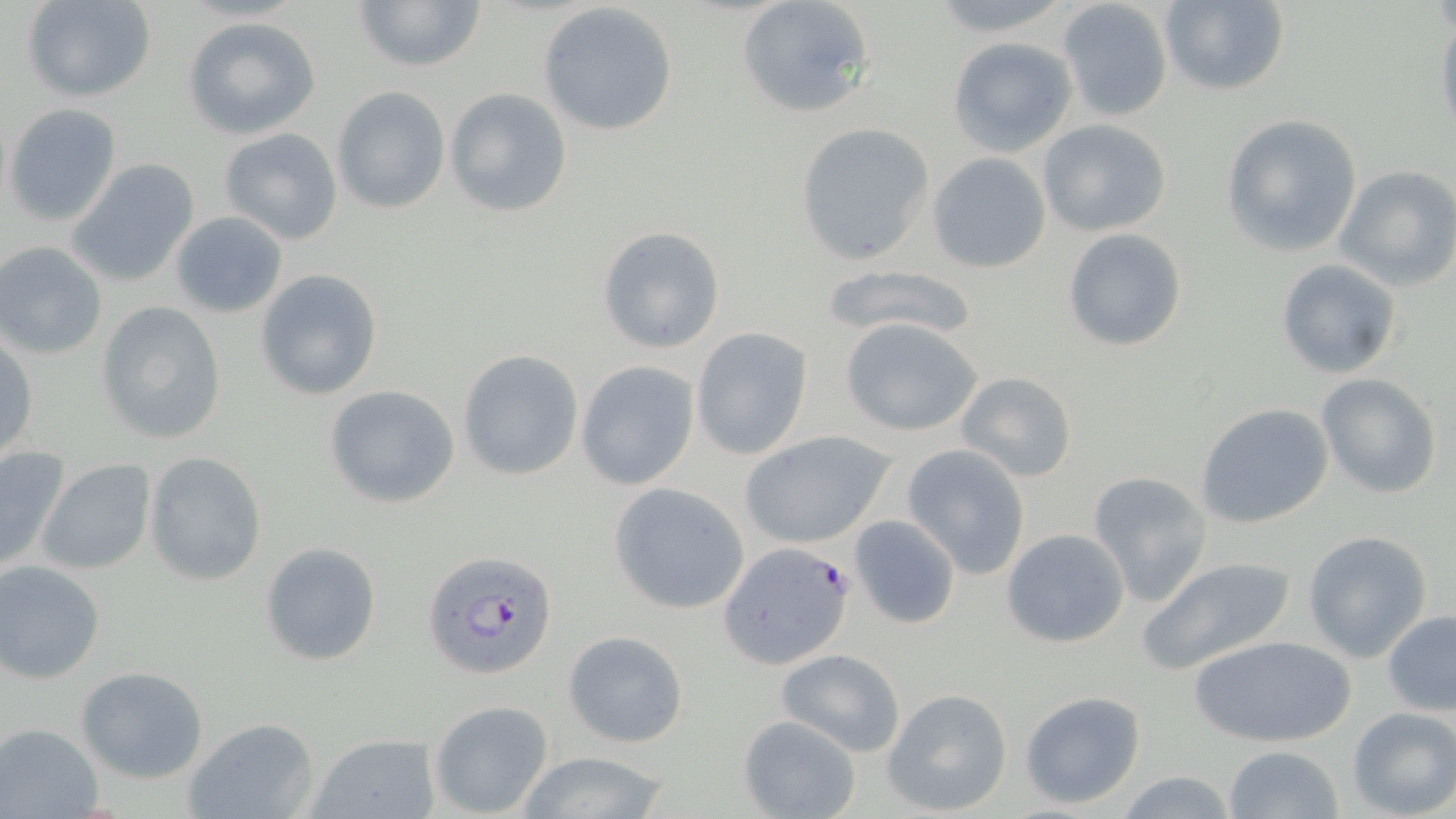
{
  "slide_level_diagnosis": "Plasmodium falciparum",
  "stain": "May-Grünwald-Giemsa",
  "image_size": "1456×819 pixels",
  "preparation": "thin blood smear",
  "uninfected_red_blood_cell_locations": "approximate bounding boxes as (x1,y1)-(x2,y2) corner pairs in pixels: (23,0)-(156,103), (351,0)-(489,74), (734,0)-(875,118), (1158,0)-(1290,96), (921,1)-(1077,35), (1057,2)-(1171,121), (537,3)-(678,137), (182,14)-(323,140), (1434,18)-(1456,142), (946,36)-(1076,156), (331,86)-(450,213), (445,88)-(574,217), (4,105)-(120,225), (1220,114)-(1364,258), (1038,120)-(1172,237), (795,122)-(934,267), (219,128)-(344,245), (926,153)-(1052,274), (67,160)-(199,287), (1334,165)-(1456,290), (169,212)-(288,317), (596,226)-(726,353), (1062,228)-(1188,353), (1,242)-(107,359), (1276,259)-(1403,381), (822,264)-(983,341), (254,269)-(384,400), (97,300)-(227,445), (840,316)-(984,437), (692,327)-(815,461), (0,336)-(37,461), (457,348)-(584,480), (574,360)-(699,490), (954,371)-(1078,484), (1316,373)-(1443,500), (323,383)-(461,509), (1194,403)-(1333,529), (738,429)-(899,549), (902,443)-(1032,578), (0,445)-(71,572), (144,453)-(266,586), (36,458)-(158,577), (1089,471)-(1212,608), (608,481)-(753,615), (848,514)-(961,630), (1000,528)-(1131,647), (1302,530)-(1433,662), (259,541)-(381,666), (1137,555)-(1296,676), (0,561)-(105,683), (1382,609)-(1456,715), (562,630)-(689,747), (1190,632)-(1353,748), (776,647)-(907,757), (76,665)-(210,782), (882,687)-(1013,816), (1019,690)-(1148,810), (429,699)-(554,817), (1346,706)-(1456,819), (737,714)-(862,819), (181,717)-(321,819), (0,724)-(104,818), (307,732)-(439,819), (1223,744)-(1345,819), (513,749)-(673,819), (1113,770)-(1241,818)",
  "magnification": "1000x",
  "field_of_view": "one of a larger specimen",
  "modality": "optical microscopy",
  "plasmodium_falciparum_infected_red_blood_cell_locations": "approximate bounding boxes as (x1,y1)-(x2,y2) corner pairs in pixels: (720,544)-(854,667), (421,549)-(558,681)"
}